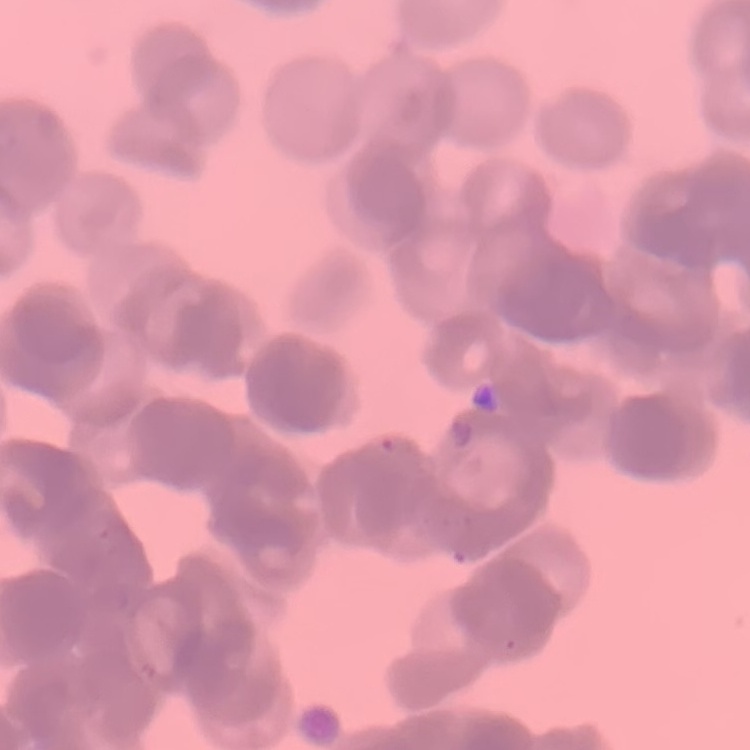
erythrocyte morphology = rouleaux formation
image type = square crop of a larger photomicrograph
preparation = thin blood film
stain = Field's or Giemsa